Assess for Plasmodium parasites.
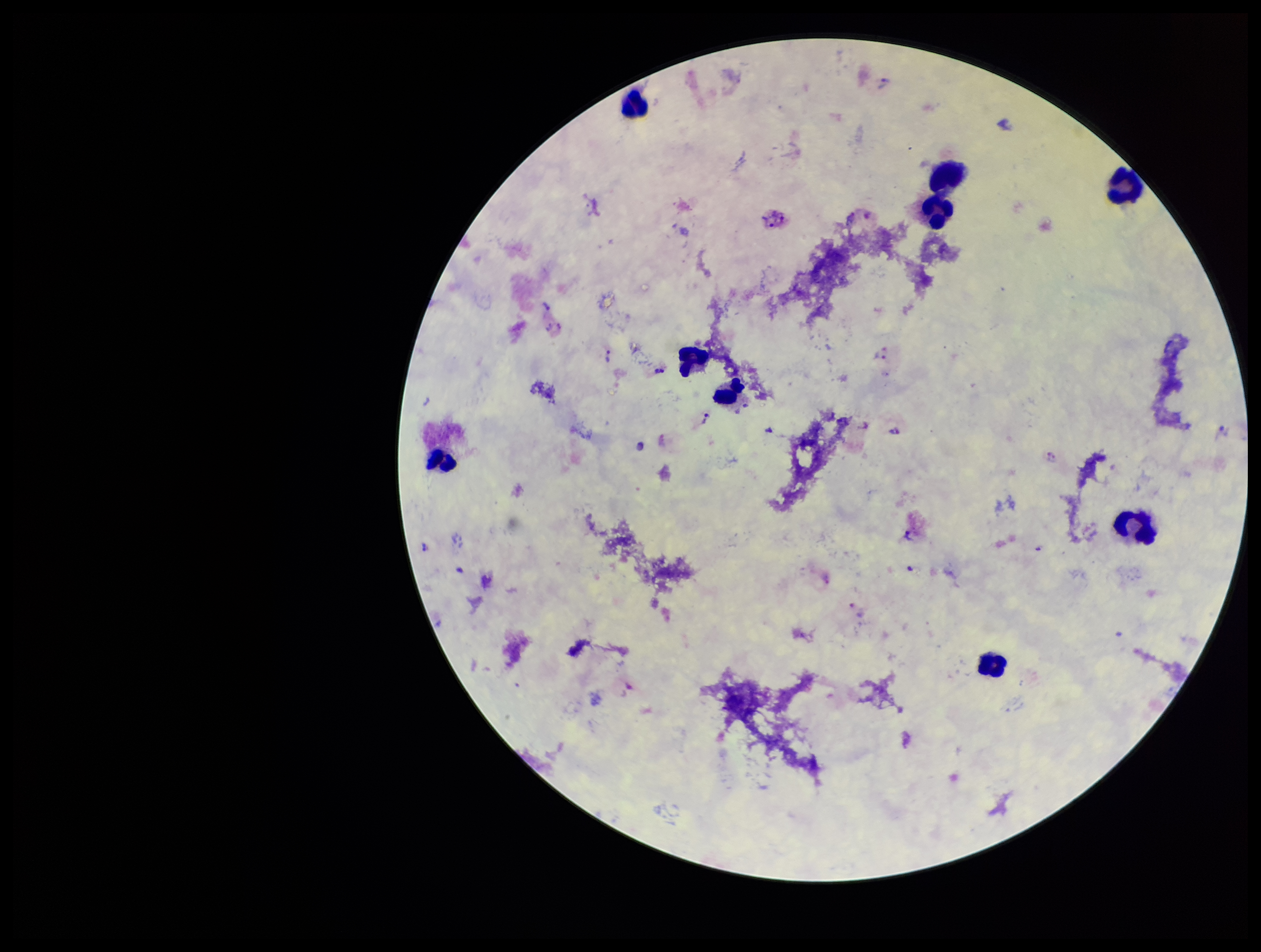
Seen.

patient malaria status = infected
capture = smartphone photograph through the microscope eyepiece
parasite count = 12
species reported for this patient = Plasmodium vivax
leukocyte count = 9
image size = 1261×952 pixels
field of view = single
preparation = thick
stain = Giemsa